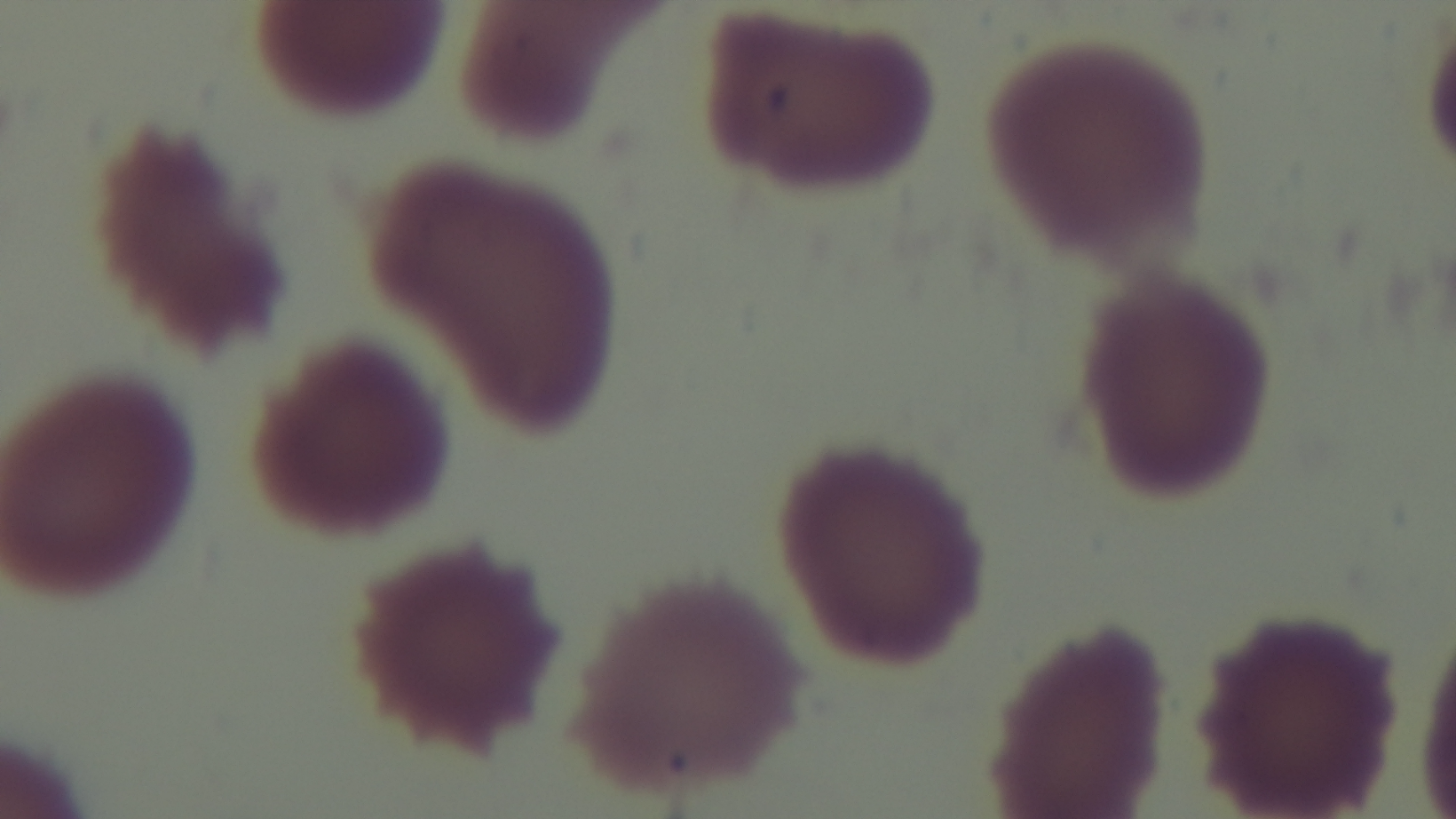

field of view = one from the slide
stain = Giemsa
capture = mounted 4K digital camera
malaria status = negative
objective = 100x oil immersion
preparation = thin
modality = light microscopy